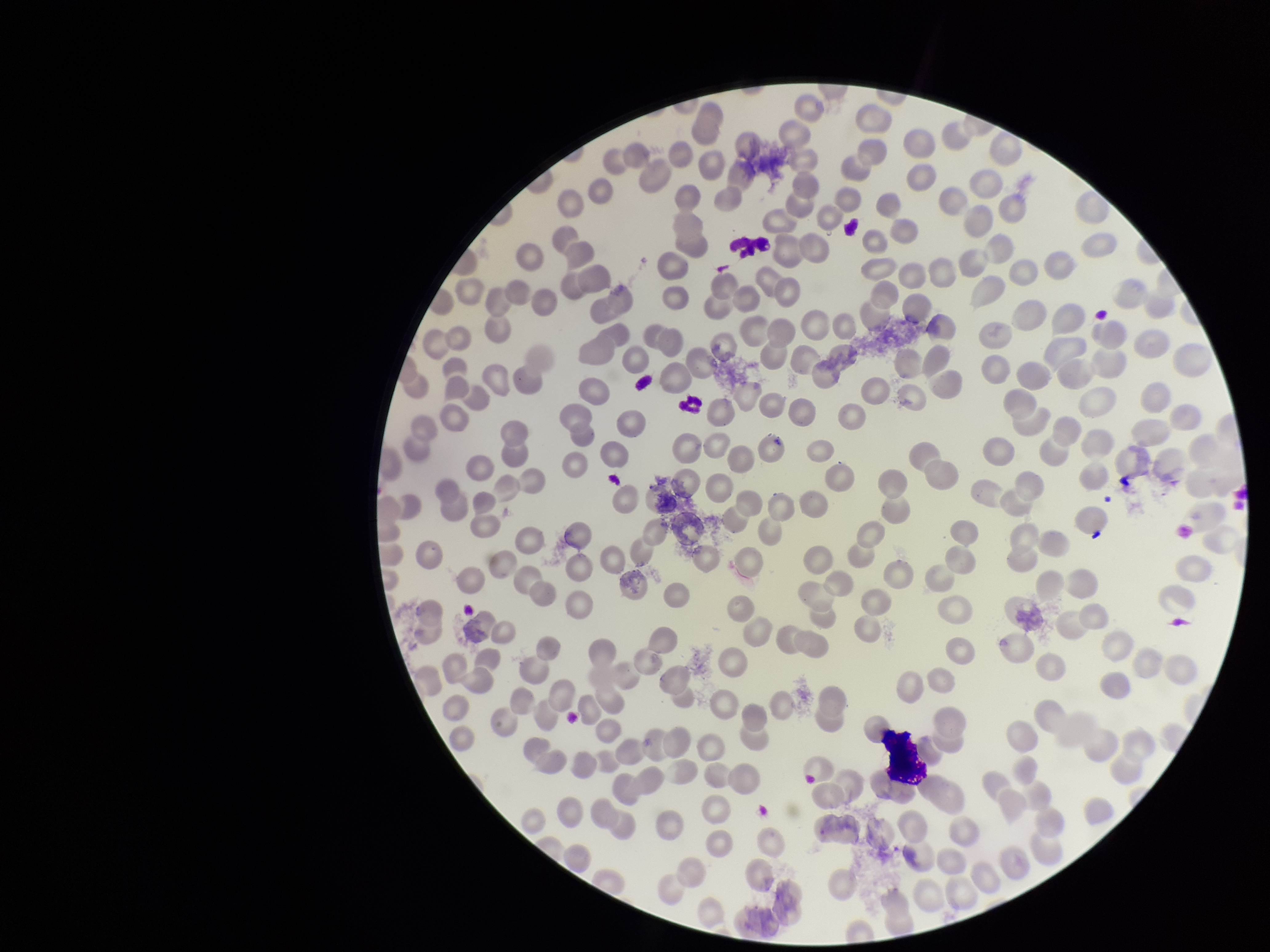
parasitized red blood cells = none seen
red blood cell count = 235
preparation = thin blood smear
stain = Giemsa
patient malaria status = negative
capture = smartphone photograph through the microscope eyepiece
field of view = single
image size = 1270×952 pixels
parasitized red blood cell count = 0